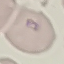 Result: malaria parasites identified. Acquired by smartphone through the microscope eyepiece. Thin blood smear. Automatically extracted cell patch, resized to 64 × 64 pixels. Giemsa-stained preparation.